Name the parasite shown.
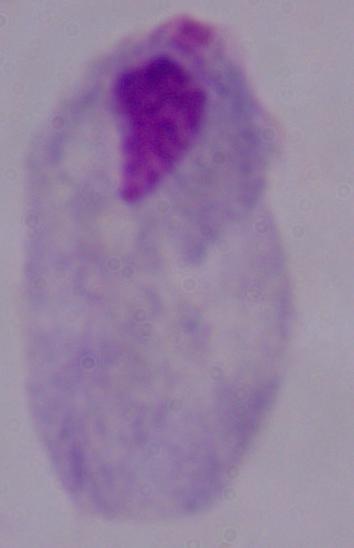
A trichomonad.

Summary:
  - Modality: photomicrograph
  - Magnification: 1000x